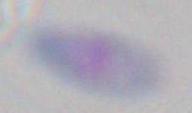
Toxoplasma gondii is seen. Captured at 1000x magnification. Photomicrograph.